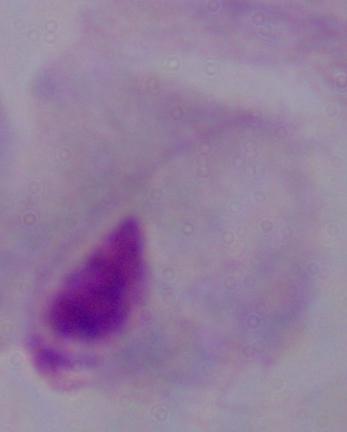

Summary:
  - Magnification: 1000x
  - Identification: trichomonad
  - Modality: photomicrograph